Locate every Plasmodium parasite.
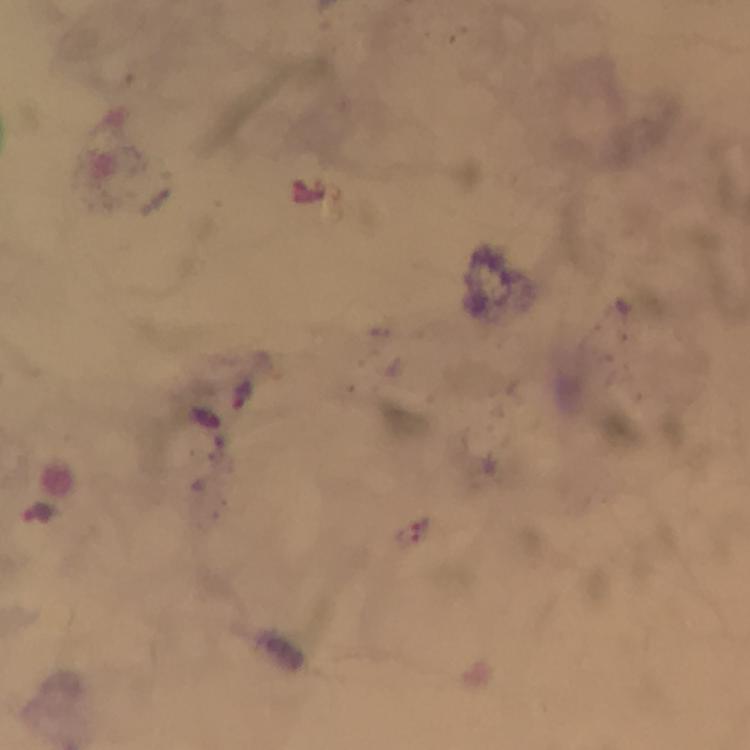
Approximate centers as [x, y] in pixels.
Plasmodium parasites: [244, 396], [206, 418], [38, 517].

Image is 750×750 pixels. Thick smear. From a malaria diagnostic workup. Cropped region of a single field of view. Giemsa stain. 100x magnification. Photographed through the microscope with a smartphone camera. Immersion oil applied.